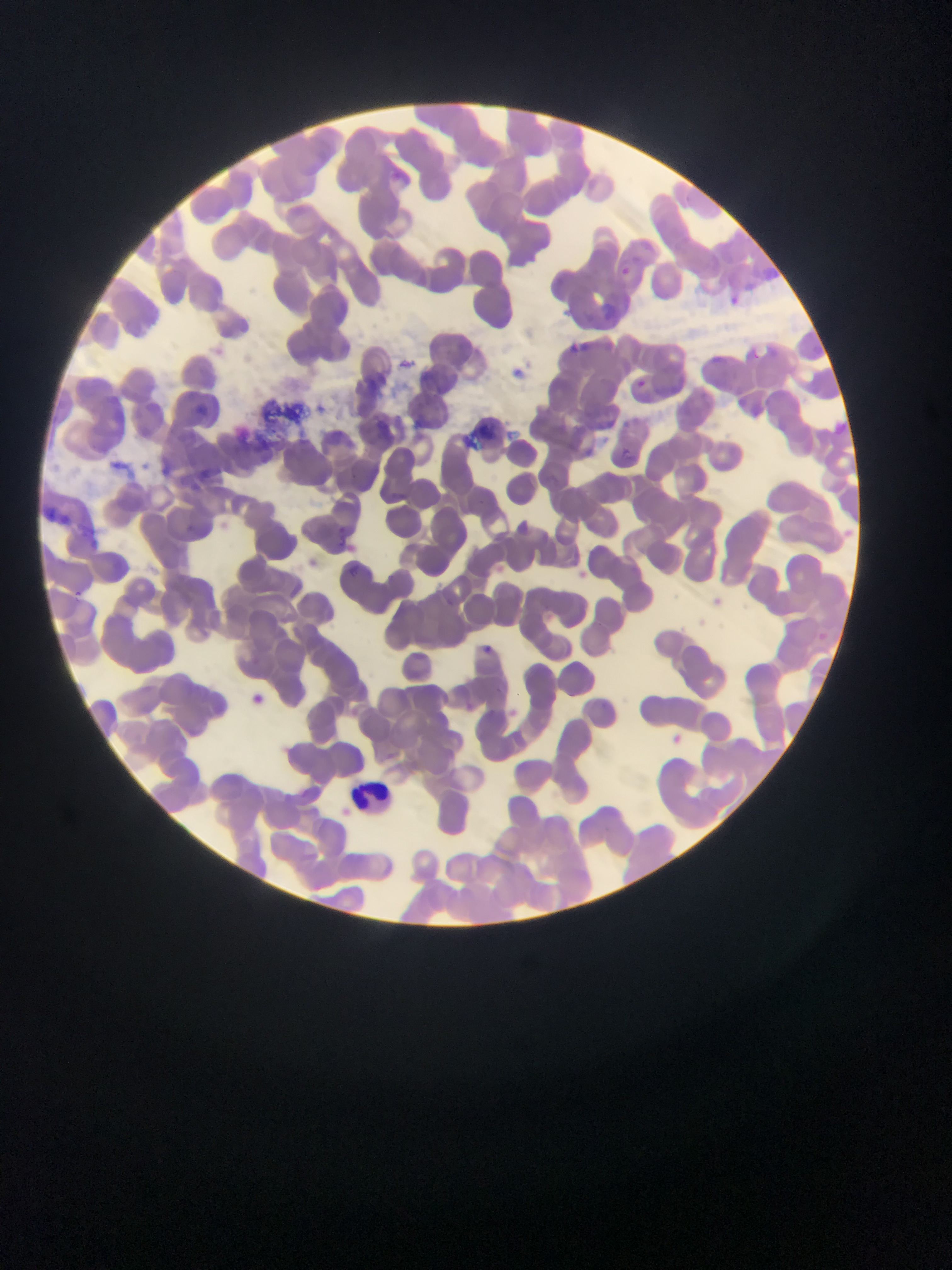

{
  "capture": "mobile-phone photograph through a microscope",
  "preparation": "thin blood smear",
  "leukocyte_locations": "approximate bounding boxes as (left, top, right, bottom) in pixels: (351, 777, 393, 814)",
  "image_size": "952×1270 pixels",
  "country": "Ghana",
  "malaria_parasite_locations": "approximate bounding boxes as (left, top, right, bottom) in pixels: (620, 262, 643, 280), (732, 292, 746, 312), (744, 344, 770, 375), (634, 379, 646, 387), (624, 447, 646, 464), (178, 523, 206, 543), (340, 562, 366, 583), (483, 640, 507, 662), (250, 693, 270, 705), (660, 724, 693, 761)",
  "field_of_view": "single"
}